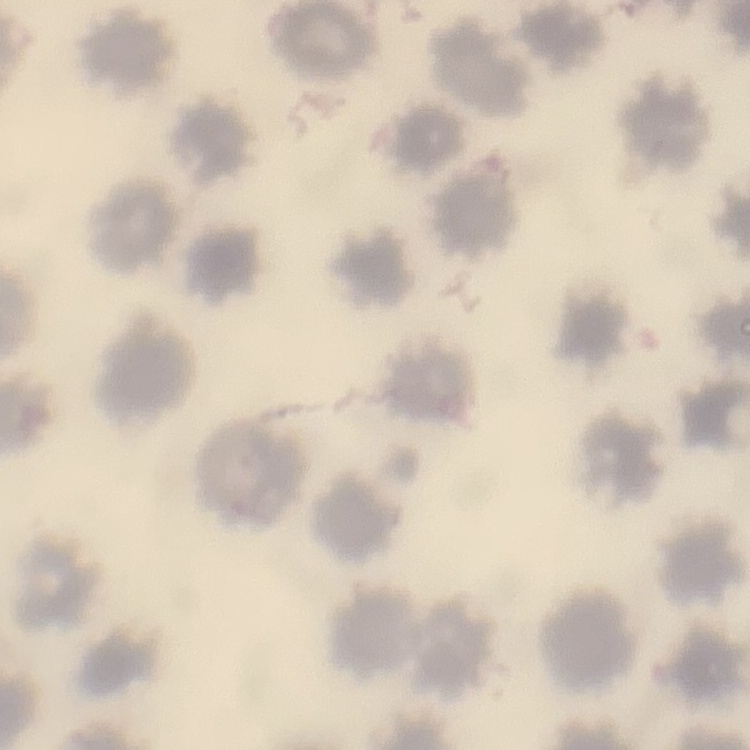
The red blood cells exhibit no rouleaux formation. Thin blood smear. Stained with either Field's or Giemsa. One tile cut from a larger photomicrograph.